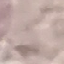
{
  "result": "negative for malaria parasites",
  "preparation": "thin smear",
  "image_type": "cell patch, automatically extracted from a larger field of view and resized to 64 × 64 pixels",
  "capture": "smartphone camera at the microscope eyepiece",
  "stain": "Giemsa"
}